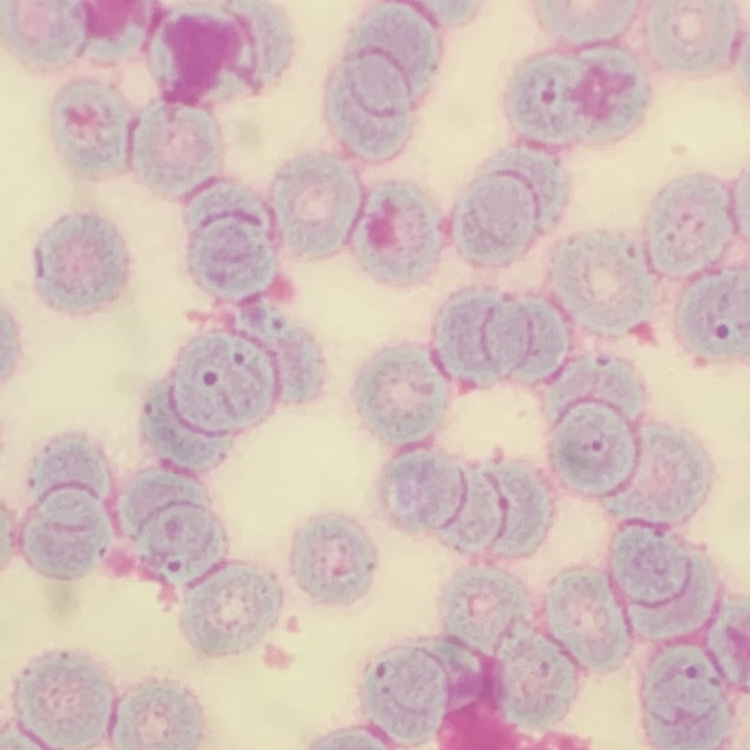

erythrocyte_morphology: rouleaux formation
image_type: one tile cut from a larger photomicrograph
preparation: thin peripheral smear
stain: Field's or Giemsa